Assess this cell for malaria.
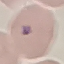

Uninfected.

Photographed with a smartphone camera at the microscope eyepiece. Thin blood smear. Giemsa stain. Automatically extracted cell patch, resized to 64 × 64 pixels.